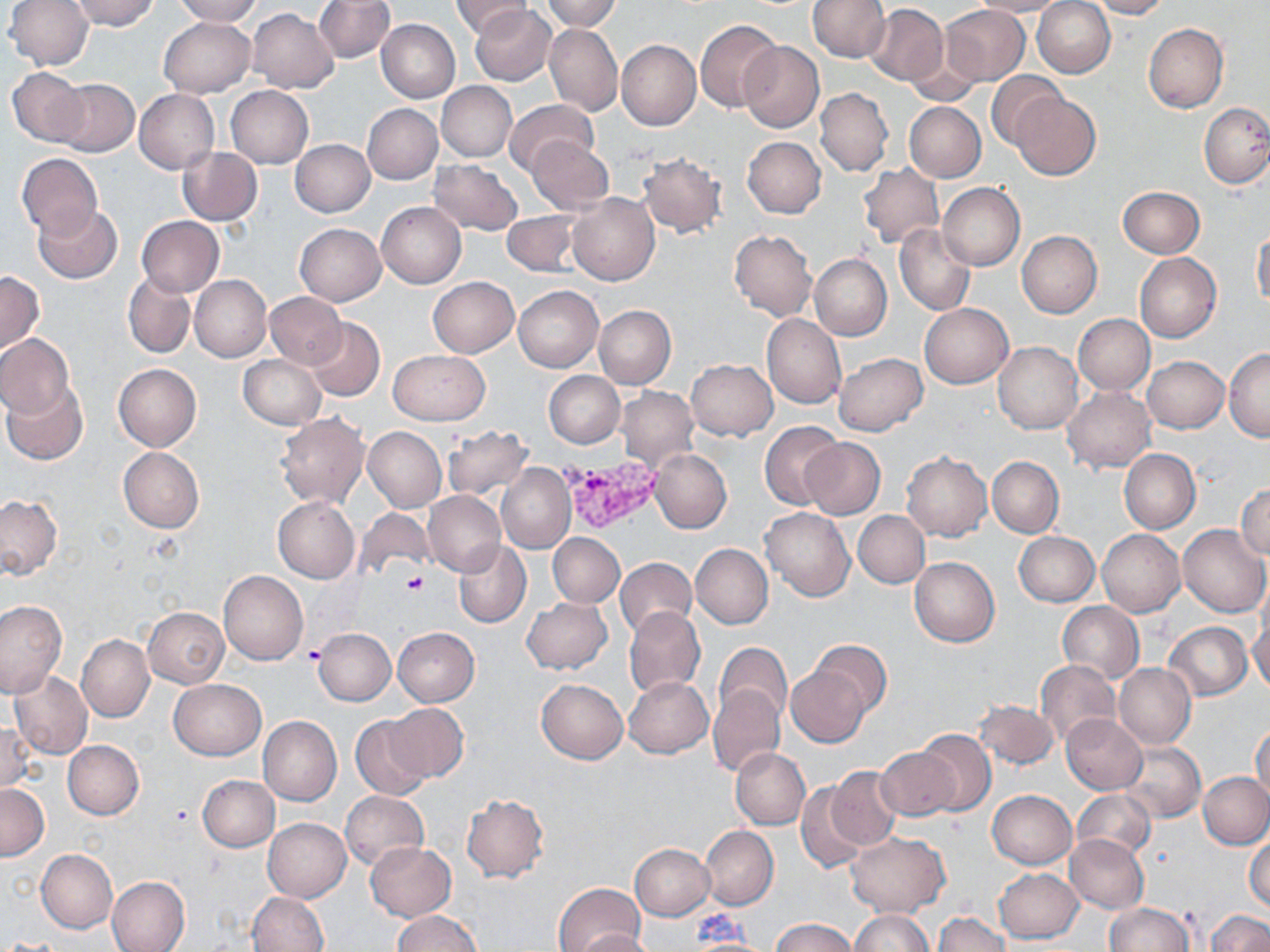
{
  "plasmodium_vivax_infected_red_blood_cell_locations": "approximate bounding boxes as (x1,y1)-(x2,y2) corner pairs in pixels: (557,454)-(665,534)",
  "slide_level_diagnosis": "Plasmodium vivax",
  "stain": "May-Grünwald-Giemsa",
  "preparation": "thin blood smear",
  "image_size": "1270×952 pixels",
  "uninfected_red_blood_cell_locations": "approximate bounding boxes as (x1,y1)-(x2,y2) corner pairs in pixels: (6,0)-(94,68), (71,0)-(159,30), (173,0)-(262,24), (313,0)-(394,62), (453,0)-(530,39), (540,0)-(622,32), (972,0)-(1068,17), (1033,0)-(1115,78), (1090,0)-(1168,18), (807,1)-(889,62), (469,4)-(557,86), (866,4)-(948,86), (940,4)-(1029,86), (312,8)-(452,78), (248,9)-(340,93), (159,17)-(256,98), (376,18)-(460,102), (696,21)-(781,112), (543,22)-(622,117), (1144,23)-(1228,112), (616,39)-(700,130), (740,42)-(824,131), (903,50)-(985,105), (7,66)-(90,148), (988,72)-(1064,150), (52,78)-(138,157), (436,82)-(517,162), (225,86)-(313,167), (814,87)-(892,177), (134,89)-(220,173), (1009,90)-(1101,180), (505,99)-(597,178), (904,101)-(986,182), (1200,102)-(1270,188), (362,103)-(443,184), (742,136)-(825,218), (529,138)-(613,213), (290,140)-(375,217), (177,147)-(262,226), (16,152)-(103,240), (638,152)-(727,238), (429,160)-(523,234), (858,163)-(944,249), (937,182)-(1025,271), (1118,185)-(1205,258), (567,192)-(659,286), (377,202)-(466,288), (33,205)-(123,283), (502,212)-(580,276), (136,216)-(224,296), (295,223)-(386,306), (894,224)-(975,316), (1251,225)-(1270,309), (729,229)-(817,320), (1017,231)-(1102,318), (809,253)-(892,340), (1135,253)-(1221,342), (123,270)-(195,359), (0,271)-(44,355), (189,275)-(271,362), (427,277)-(519,357), (514,285)-(604,373), (265,293)-(346,366), (919,303)-(1012,388), (594,305)-(676,389), (762,313)-(846,410), (1074,313)-(1155,395), (304,317)-(385,401), (0,333)-(75,418), (994,341)-(1083,433), (388,349)-(490,425), (1224,349)-(1270,440), (834,352)-(928,436), (239,354)-(325,430), (1142,356)-(1229,433), (687,359)-(777,440), (113,364)-(202,451), (543,371)-(625,448), (0,381)-(87,465), (616,387)-(699,469), (1063,387)-(1155,472), (276,413)-(369,509), (759,420)-(842,510), (441,425)-(533,501), (363,427)-(447,512), (800,437)-(884,520), (118,447)-(204,532), (649,448)-(732,534), (1119,449)-(1201,533), (901,452)-(992,541), (988,456)-(1064,537), (496,463)-(576,554), (1235,483)-(1270,560), (424,490)-(506,577), (0,496)-(61,579), (273,499)-(360,581), (760,506)-(855,602), (357,509)-(435,580), (853,511)-(930,588), (1178,524)-(1270,618), (1098,529)-(1185,618), (1013,531)-(1098,606), (548,533)-(625,607), (453,540)-(531,628), (690,543)-(773,628), (910,556)-(1000,646), (615,559)-(696,639), (219,570)-(308,665), (522,598)-(612,674), (0,601)-(66,697), (1056,601)-(1144,684), (624,606)-(705,698), (143,607)-(228,688), (1248,614)-(1270,693), (1164,622)-(1253,700), (392,627)-(480,706), (314,628)-(395,705), (76,635)-(154,722), (810,639)-(891,715), (714,642)-(793,725), (1036,659)-(1121,748), (1114,662)-(1196,748), (786,665)-(871,747), (9,671)-(92,760), (624,677)-(712,758), (536,678)-(628,764), (169,679)-(266,760), (708,684)-(784,777), (974,700)-(1057,769), (385,703)-(468,782), (1061,714)-(1147,794), (349,715)-(431,800), (258,717)-(341,805), (1,720)-(37,794), (1251,724)-(1270,805), (915,728)-(996,816), (63,740)-(144,819), (1119,740)-(1204,822), (731,748)-(810,829), (877,748)-(957,820), (827,767)-(901,850), (1199,772)-(1270,849), (198,775)-(280,852), (797,781)-(868,872), (0,783)-(49,861), (987,789)-(1076,869), (1072,789)-(1155,860), (340,790)-(429,870), (462,794)-(549,883), (263,817)-(351,903), (700,826)-(778,910), (846,833)-(951,917), (1065,833)-(1149,914), (1246,835)-(1270,913), (364,843)-(456,921), (630,844)-(715,920), (36,850)-(117,933), (994,868)-(1083,944), (107,876)-(189,952), (553,883)-(645,952), (247,891)-(328,952), (1105,902)-(1192,952), (1206,909)-(1270,952), (850,910)-(931,951), (393,911)-(483,952), (933,912)-(1011,952), (771,918)-(857,952), (573,929)-(656,952)",
  "field_of_view": "single",
  "platelet_locations": "approximate bounding boxes as (x1,y1)-(x2,y2) corner pairs in pixels: (398,571)-(428,597), (301,644)-(326,666)",
  "modality": "optical microscopy",
  "magnification": "1000x"
}